State which parasite is depicted.
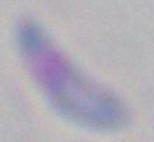
Toxoplasma gondii.

Summary:
  - Modality: photomicrograph
  - Magnification: 1000x